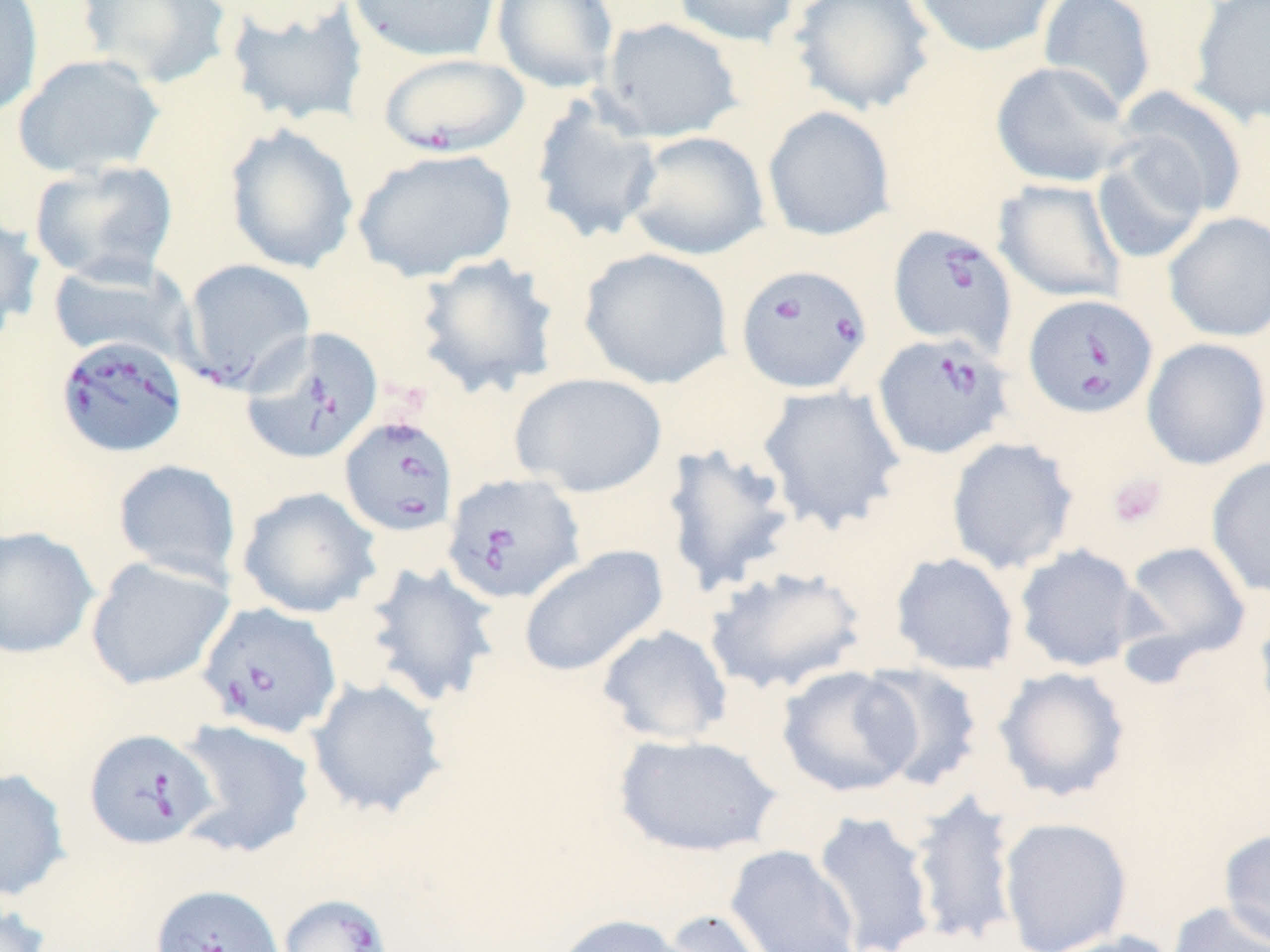
Approximate bounding boxes as [x1, y1, x2, y2] in pixels. Babesia divergens-infected red blood cell locations: [378, 52, 529, 157], [888, 223, 1018, 355], [180, 258, 317, 392], [735, 263, 873, 394], [1022, 293, 1158, 419], [240, 327, 383, 465], [872, 332, 1014, 460], [54, 334, 189, 459], [339, 414, 459, 537], [442, 472, 585, 604], [197, 601, 342, 739], [84, 728, 218, 850], [150, 884, 284, 952], [277, 893, 395, 952]. Uninfected red blood cell locations: [0, 0, 44, 118], [75, 0, 233, 89], [348, 0, 501, 62], [491, 0, 619, 93], [671, 0, 801, 47], [788, 0, 936, 116], [910, 0, 1059, 58], [1037, 0, 1157, 115], [223, 1, 369, 128], [1188, 1, 1269, 127], [599, 17, 743, 142], [12, 53, 166, 179], [991, 61, 1134, 188], [1114, 87, 1248, 219], [530, 94, 663, 245], [762, 105, 896, 241], [224, 123, 360, 274], [625, 130, 769, 261], [1091, 139, 1211, 265], [351, 148, 517, 283], [29, 159, 179, 286], [993, 179, 1126, 304], [0, 210, 46, 340], [1163, 212, 1270, 342], [578, 247, 733, 389], [413, 253, 561, 399], [47, 258, 194, 364], [1141, 337, 1270, 470], [509, 371, 668, 497], [756, 384, 907, 534], [945, 436, 1080, 575], [660, 441, 798, 596], [1206, 456, 1270, 597], [112, 458, 242, 586], [236, 486, 381, 619], [0, 525, 99, 659], [1119, 540, 1252, 668], [1014, 543, 1145, 673], [517, 545, 669, 678], [889, 551, 1020, 676], [85, 556, 234, 690], [360, 560, 502, 709], [703, 564, 869, 696], [1253, 596, 1270, 728], [596, 624, 733, 746], [856, 662, 986, 791], [776, 665, 921, 798], [992, 666, 1132, 802], [307, 677, 448, 819], [172, 719, 316, 859], [612, 733, 783, 857], [0, 767, 71, 902], [907, 787, 1022, 947], [811, 810, 938, 951], [997, 817, 1132, 952], [1218, 826, 1270, 949], [725, 845, 862, 952], [0, 898, 52, 952], [1166, 900, 1270, 952], [655, 908, 775, 952], [550, 912, 691, 952], [1034, 932, 1186, 952]. Platelet locations: [1107, 472, 1168, 528]. Slide-level diagnosis: Babesia divergens. Single field of view. Captured at 1000x magnification. Light microscopy. Thin blood film. Image is 1270×952 pixels. May-Grünwald-Giemsa-stained preparation.